Outline each uninfected red blood cell.
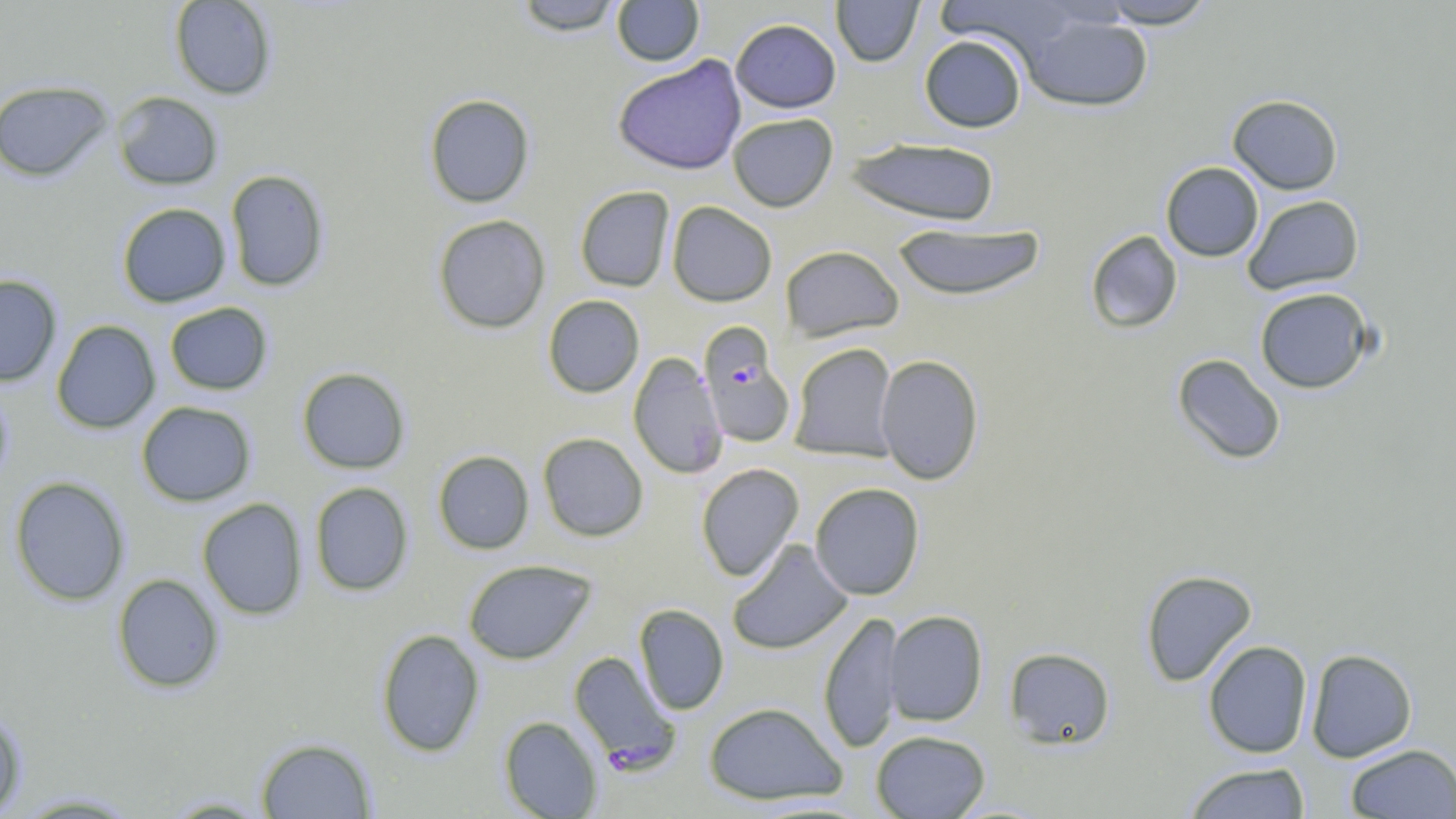
Approximate bounding boxes as [x1, y1, x2, y2] in pixels.
Uninfected red blood cells: [169, 0, 277, 100], [513, 0, 622, 35], [612, 0, 705, 66], [831, 0, 924, 67], [1096, 0, 1217, 29], [935, 1, 1086, 65], [1017, 11, 1154, 113], [730, 18, 841, 113], [919, 34, 1027, 132], [612, 55, 747, 175], [0, 80, 113, 181], [112, 91, 224, 190], [424, 94, 535, 208], [1227, 94, 1343, 195], [727, 113, 838, 212], [845, 137, 1000, 225], [1160, 161, 1264, 262], [225, 169, 330, 291], [575, 186, 675, 292], [1242, 194, 1364, 295], [667, 201, 777, 306], [117, 202, 231, 307], [432, 214, 551, 333], [891, 222, 1046, 301], [1085, 230, 1183, 334], [780, 245, 904, 341], [0, 274, 62, 386], [1254, 287, 1375, 394], [543, 295, 644, 397], [164, 302, 273, 395], [51, 320, 161, 434], [789, 342, 898, 462], [628, 352, 727, 480], [1172, 353, 1286, 465], [876, 354, 985, 485], [296, 367, 411, 474], [0, 383, 14, 493], [136, 401, 256, 506], [537, 432, 649, 541], [433, 450, 534, 554], [695, 463, 804, 581], [9, 476, 130, 606], [309, 482, 414, 596], [810, 482, 925, 599], [197, 498, 308, 620], [727, 540, 852, 655], [463, 559, 596, 664], [1140, 569, 1258, 687], [112, 573, 225, 693], [634, 604, 729, 715], [885, 609, 987, 726], [818, 611, 901, 754], [376, 629, 485, 757], [1203, 640, 1313, 759], [1004, 647, 1116, 750], [1305, 648, 1418, 762], [704, 701, 846, 805], [0, 706, 27, 816], [499, 716, 603, 818], [871, 729, 990, 818], [255, 737, 377, 818], [1344, 744, 1456, 818], [1182, 762, 1311, 819], [8, 792, 147, 817], [158, 795, 278, 817].

slide_level_diagnosis: Plasmodium falciparum
field_of_view: one of a larger specimen
modality: optical microscopy
plasmodium_falciparum_infected_red_blood_cell_locations: 'approximate bounding boxes as [x1, y1, x2, y2] in pixels: [698, 324, 796, 448], [568, 650, 678, 770]'
stain: May-Grünwald-Giemsa
image_size: 1456×819 pixels
magnification: 1000x
preparation: thin blood smear